Classify this cell by malaria status.
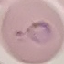
Parasitized.

Giemsa-stained preparation. Photographed with a smartphone camera at the microscope eyepiece. Automatically extracted cell patch, resized to 64 × 64 pixels. Thin blood smear.